Report the malaria status of this cell.
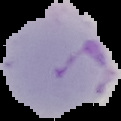

It is parasitized.

Summary:
  - Image size: 121×121 pixels
  - Image type: segmented cell region on a black background
  - Preparation: thin blood film